Outline each Plasmodium falciparum-infected red blood cell.
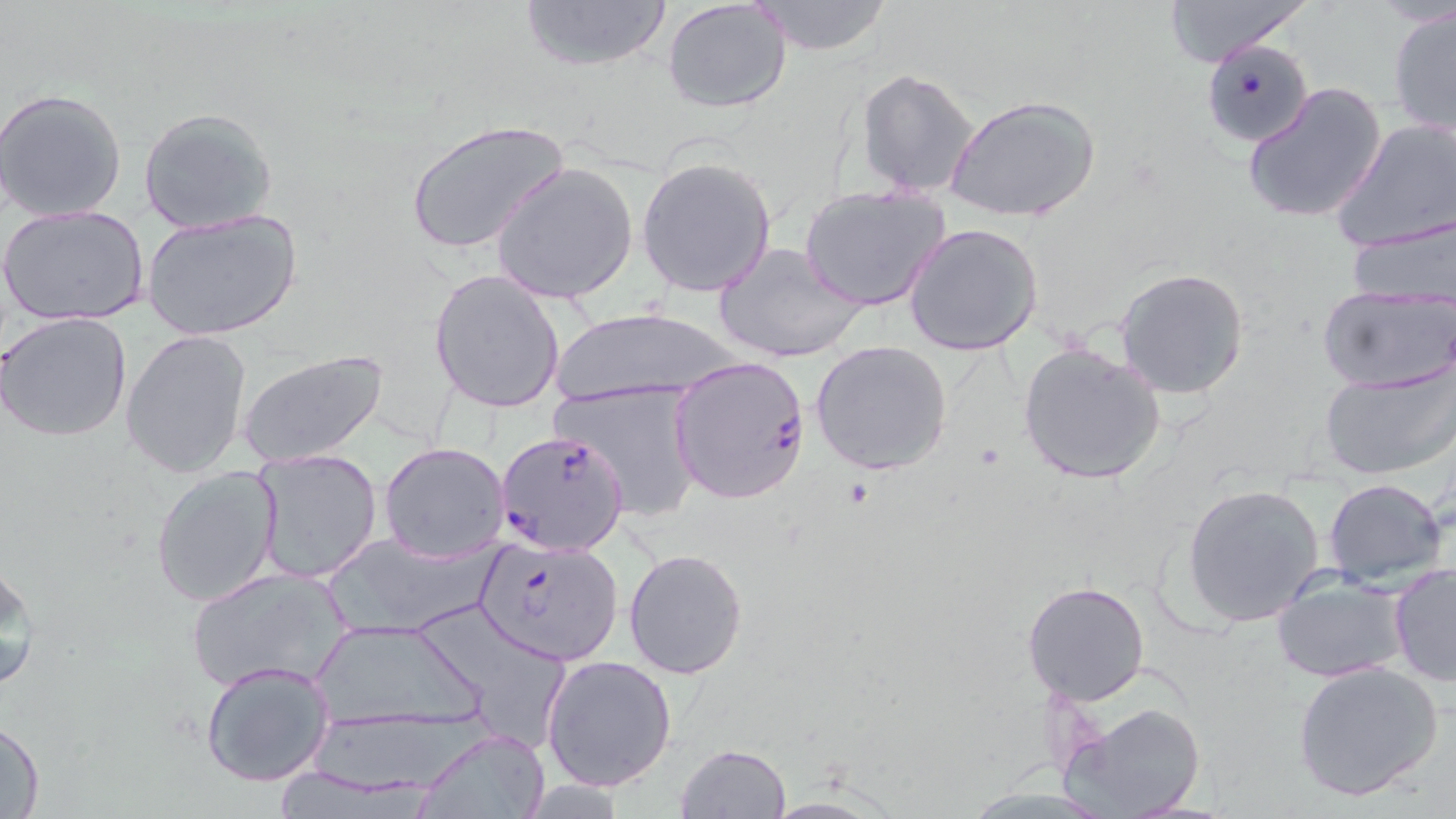

Approximate bounding boxes as (x1,y1)-(x2,y2) corner pairs in pixels.
Plasmodium falciparum-infected red blood cells: (1203,39)-(1312,145), (668,356)-(811,506), (497,429)-(631,556), (474,535)-(624,665).

Summary:
  - Uninfected red blood cell locations: (517,0)-(673,73), (750,0)-(894,56), (1157,0)-(1313,67), (662,1)-(793,115), (1387,4)-(1456,137), (856,68)-(980,196), (1243,82)-(1386,224), (0,88)-(128,223), (947,94)-(1102,224), (136,106)-(278,236), (1333,118)-(1456,253), (404,119)-(568,256), (637,156)-(776,298), (491,162)-(638,306), (800,186)-(950,310), (1,203)-(151,326), (141,209)-(304,343), (1347,217)-(1456,310), (902,222)-(1044,357), (714,240)-(866,364), (1115,267)-(1250,398), (428,269)-(566,415), (1317,286)-(1455,392), (551,308)-(741,405), (0,312)-(132,443), (121,329)-(252,478), (810,339)-(954,474), (1018,343)-(1168,486), (236,351)-(390,469), (1319,365)-(1454,481), (556,382)-(705,520), (379,441)-(511,563), (249,448)-(384,585), (150,465)-(282,609), (1323,477)-(1449,587), (1182,483)-(1326,626), (319,530)-(494,639), (624,549)-(749,679), (0,557)-(41,695), (1390,563)-(1456,685), (184,566)-(354,695), (1272,572)-(1409,683), (1022,577)-(1152,705), (430,607)-(568,749), (305,618)-(491,741), (542,656)-(677,793), (199,659)-(335,788), (1292,660)-(1445,803), (1071,702)-(1208,817), (2,717)-(45,818), (415,729)-(551,818), (674,743)-(793,818), (758,795)-(900,819)
  - Slide-level diagnosis: Plasmodium falciparum
  - Stain: May-Grünwald-Giemsa
  - Magnification: 1000x
  - Field of view: one of a larger specimen
  - Preparation: thin blood smear
  - Image size: 1456×819 pixels
  - Modality: light microscopy